Comment on the morphology of the erythrocytes.
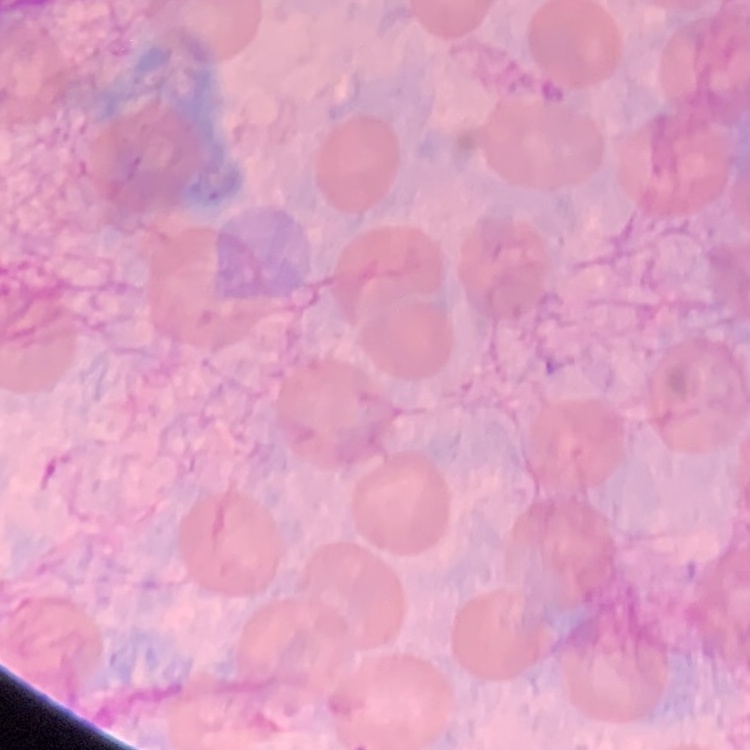
They show no rouleaux formation.

Square crop of a larger photomicrograph. Thin peripheral smear. Stained with either Field's or Giemsa.